Assess the morphology of the red blood cells.
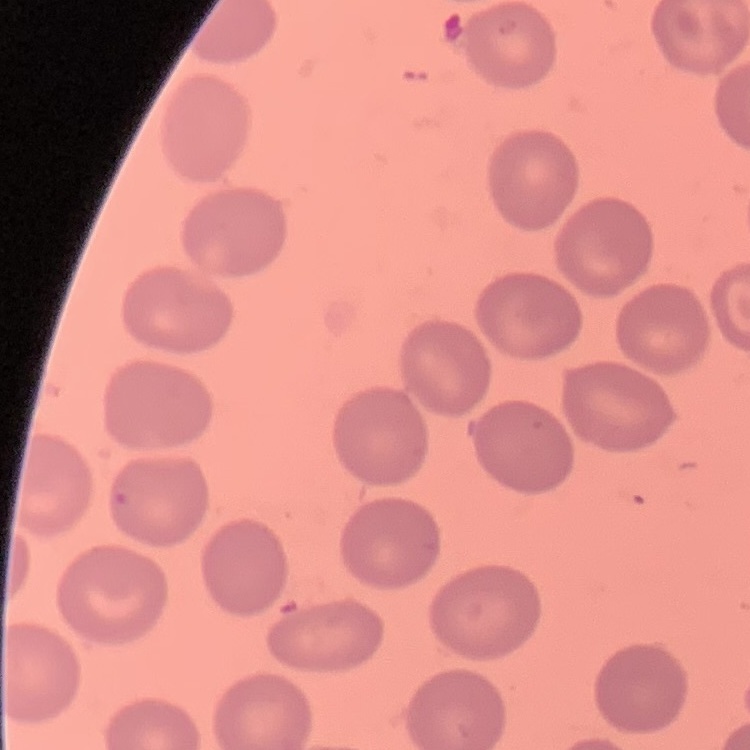

They show no rouleaux formation.

image_type: one tile cut from a larger photomicrograph
stain: Field's or Giemsa
preparation: thin blood smear